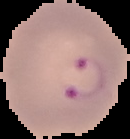
Summary:
  - Image size: 130×139 pixels
  - Preparation: thin blood smear
  - Image type: segmented cell region on a black background
  - Malaria status: parasitized